Report the malaria status of this cell.
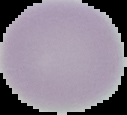
It is uninfected.

image_type: segmented cell region on a black background
preparation: thin blood film
image_size: 127×115 pixels